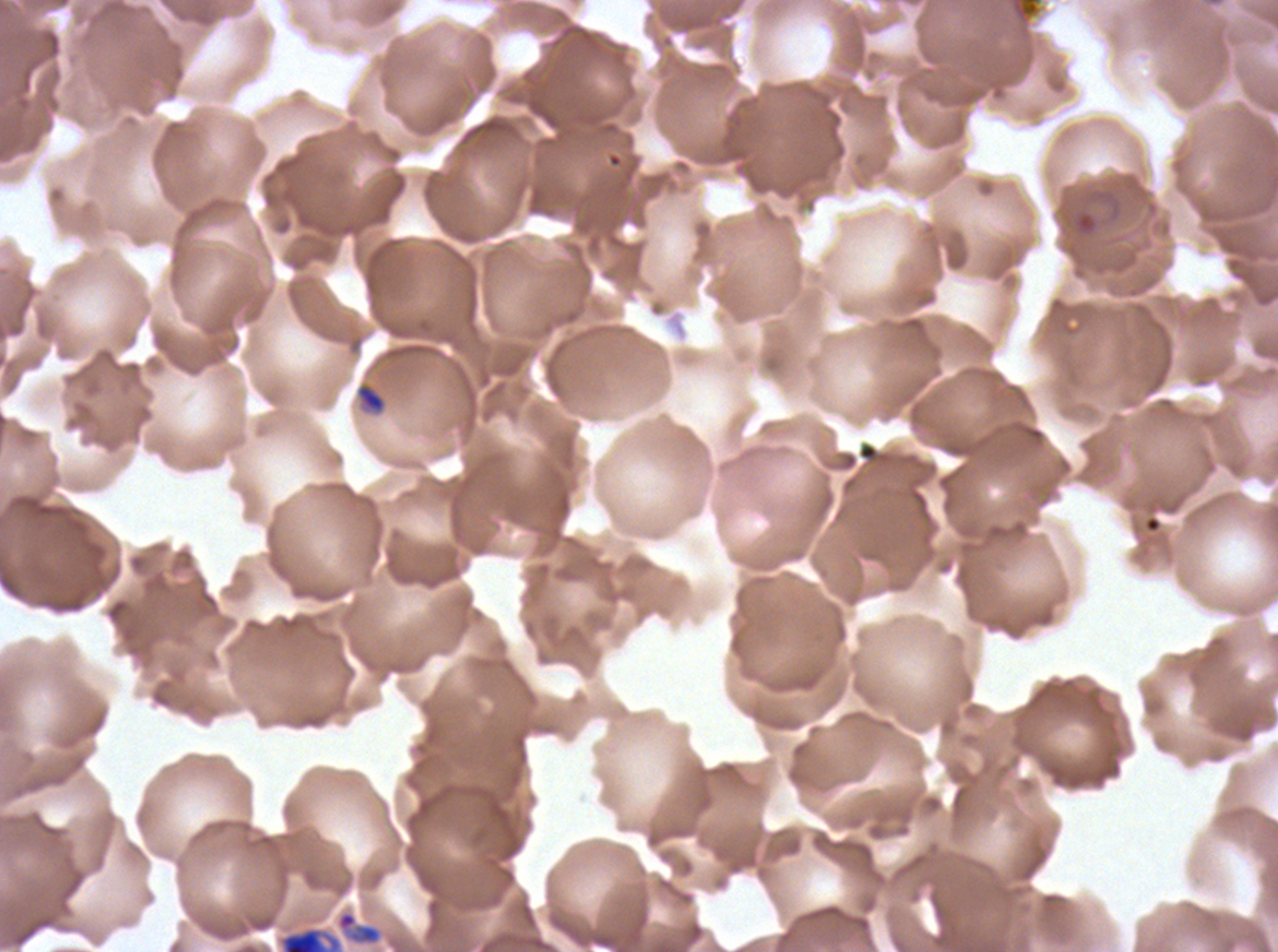

preparation: thin blood film
image_size: 1278×952 pixels
stain: Giemsa
specimen: ex-vivo Plasmodium falciparum culture from a patient in The Gambia, grown for 24 to 48 hours
late_ring_early_trophozoite_locations: 'approximate bounding boxes as (x1, y1, x2, y2) in pixels: (357, 384, 386, 412), (278, 926, 342, 951)'
life_cycle_stages_observed: ring, late-ring/early-trophozoite
field_of_view: one sub-image of a larger composite
ring_locations: 'approximate bounding boxes as (x1, y1, x2, y2) in pixels: (1073, 211, 1099, 236)'